Give the position of every Plasmodium parasite.
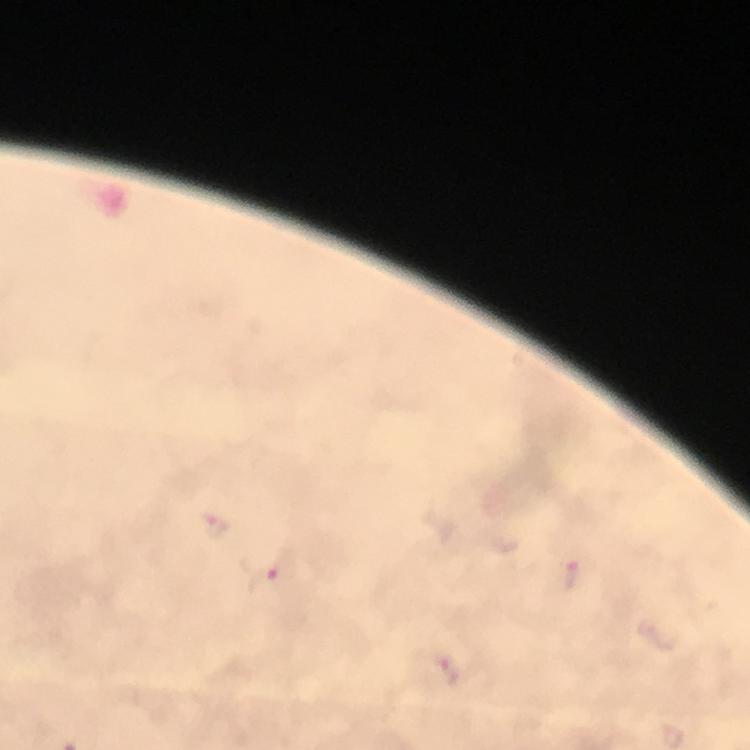

Approximate centers as {x, y} in pixels.
Plasmodium parasites: {215, 528}, {269, 576}.

magnification = 100x
immersion oil = applied
stain = Giemsa
capture = smartphone photograph through a microscope
cropped from = one field of view
context = from a malaria diagnostic workup
image size = 750×750 pixels
preparation = thick blood smear